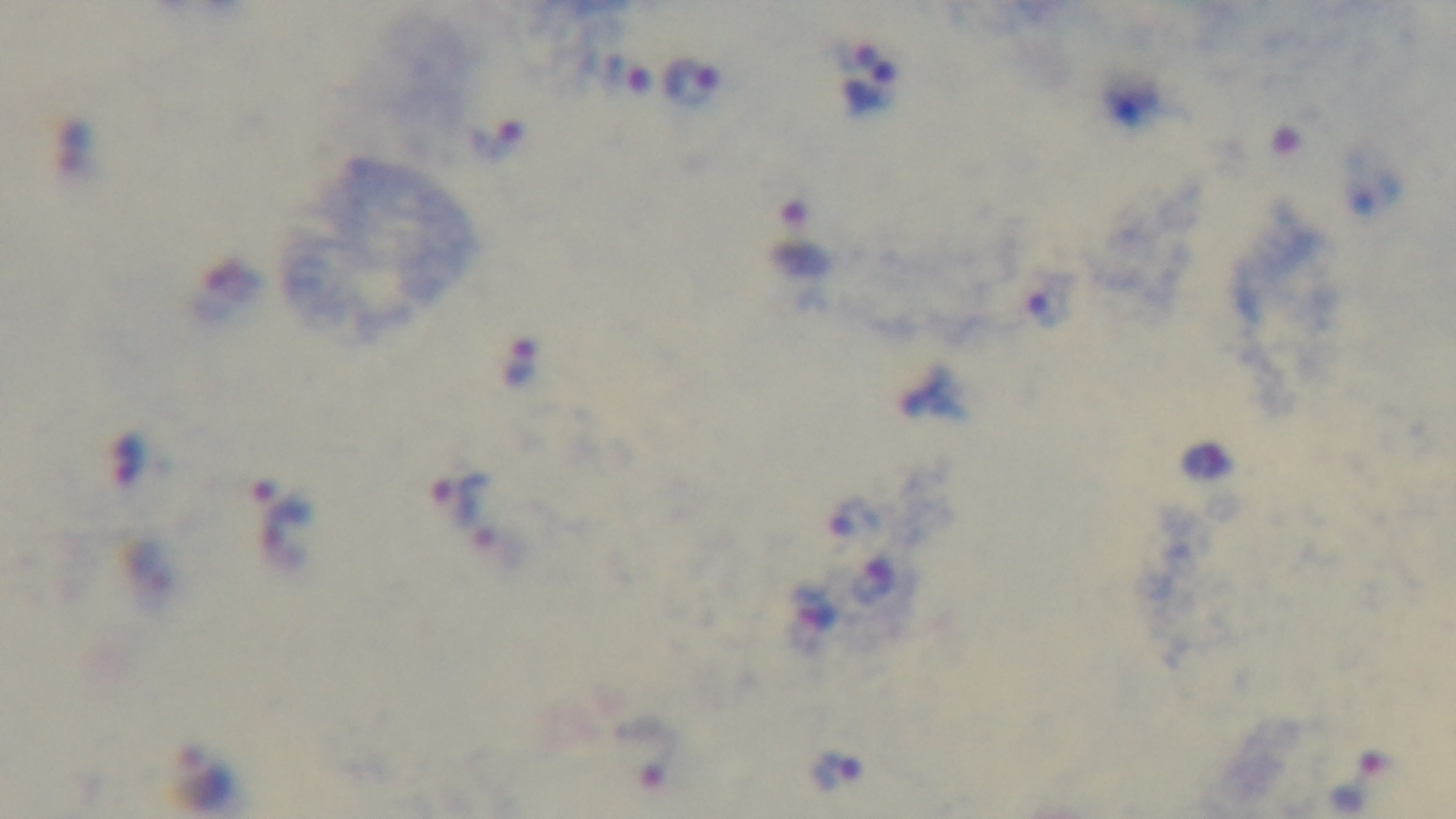
modality: light microscopy
preparation: thick smear
malaria_status: infected
field_of_view: one from the slide
capture: mounted 4K digital camera
objective: 100x oil immersion
stain: Giemsa